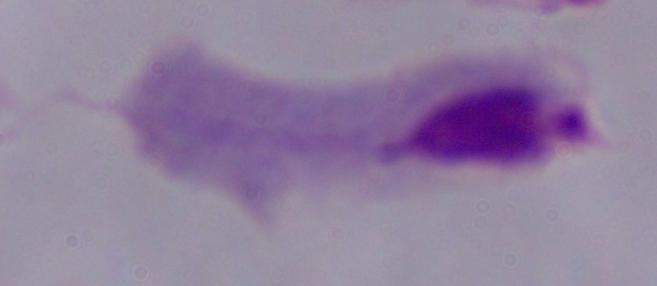

magnification = 1000x
identification = trichomonad
modality = micrograph